Locate every Plasmodium parasite.
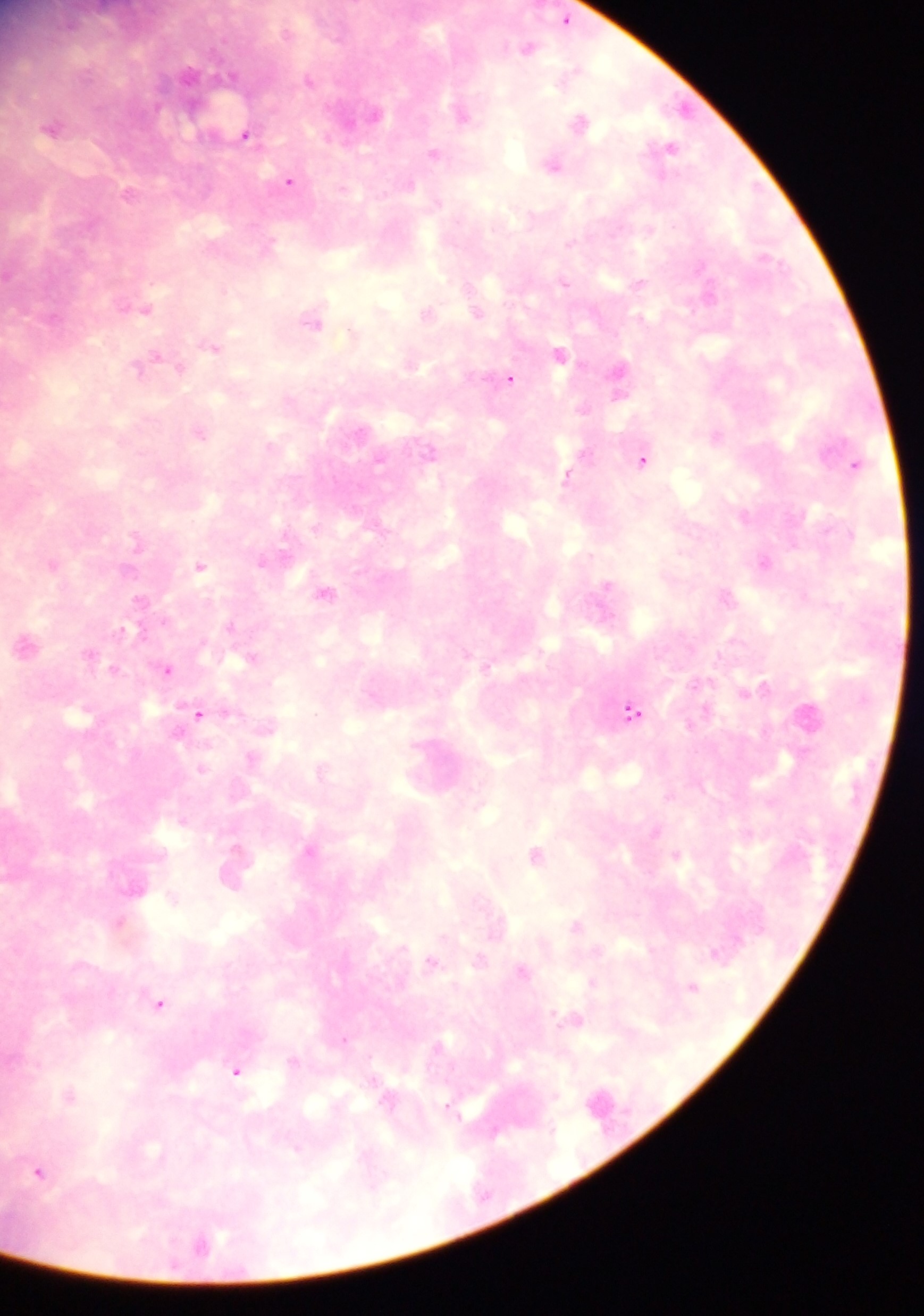
Approximate centers as {x, y} in pixels.
Plasmodium parasites: {565, 19}, {526, 47}, {309, 79}, {683, 108}, {462, 111}, {373, 113}, {581, 121}, {52, 126}, {246, 134}, {668, 147}, {434, 153}, {553, 163}, {289, 181}, {129, 191}, {638, 283}, {143, 307}, {476, 311}, {427, 313}, {313, 320}, {352, 334}, {212, 344}, {559, 354}, {153, 359}, {409, 361}, {618, 375}, {509, 378}, {200, 432}, {716, 435}, {643, 458}, {855, 464}, {567, 475}, {745, 515}, {262, 561}, {765, 562}, {55, 563}, {200, 566}, {324, 592}, {726, 595}, {141, 601}, {26, 643}, {252, 656}, {167, 668}, {760, 687}, {632, 712}, {198, 713}, {808, 715}, {252, 757}, {321, 770}, {309, 850}, {536, 854}, {234, 866}, {173, 897}, {121, 921}, {576, 925}, {432, 961}, {522, 971}, {592, 982}, {692, 986}, {160, 1003}, {574, 1018}, {439, 1046}, {238, 1071}, {71, 1095}, {40, 1171}, {202, 1243}.

country: Ghana
field_of_view: single
preparation: thick blood film
capture: mobile-phone photograph through a microscope
image_size: 924×1316 pixels